State which cell type is depicted.
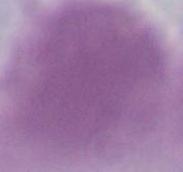

This is an erythrocyte.

Summary:
  - Magnification: 1000x
  - Modality: photomicrograph